Outline malaria parasites and classify them by life-cycle stage.
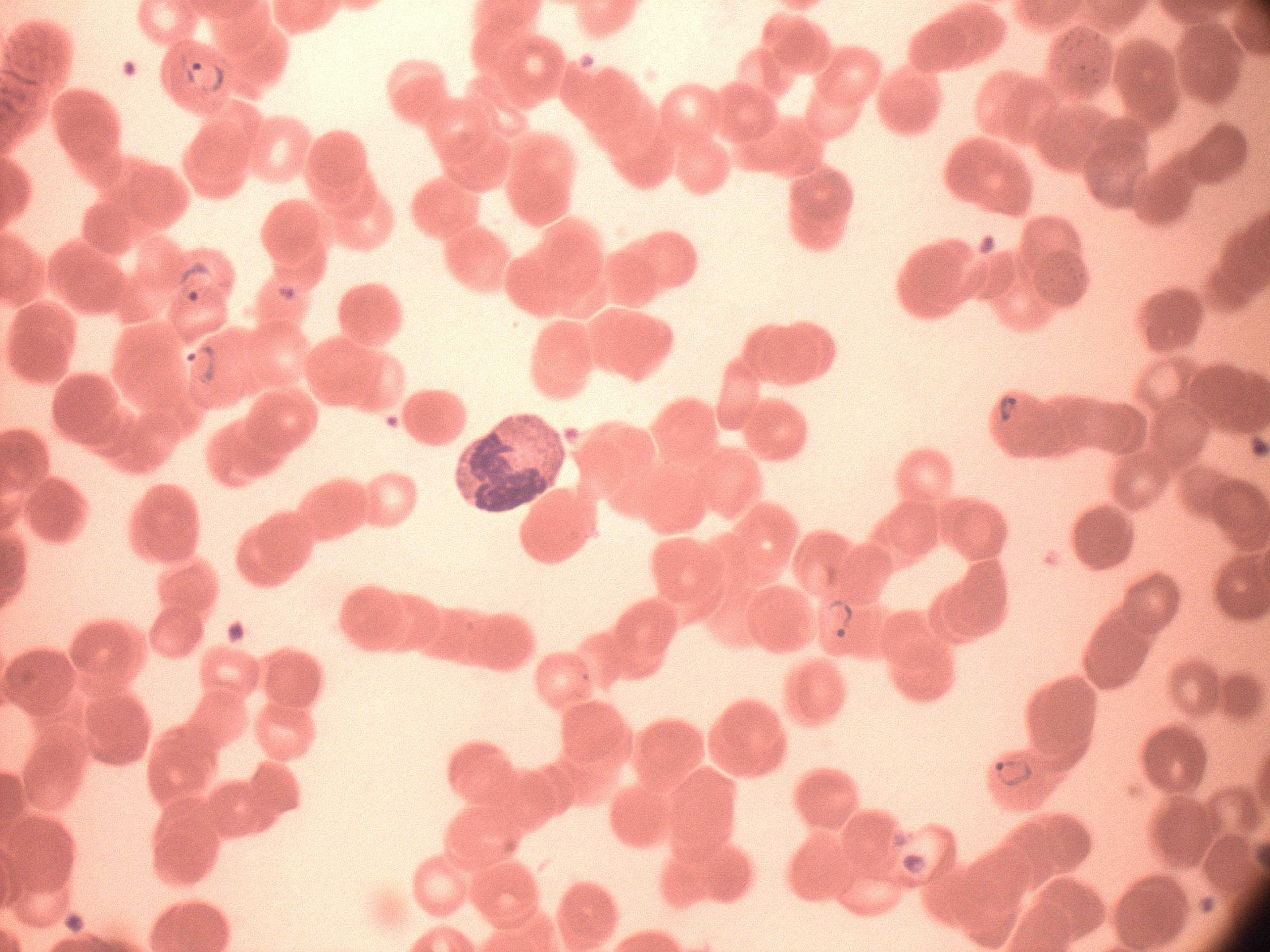
Approximate bounding boxes as (x1,y1)-(x2,y2) corner pairs in pixels, from the source annotation, which is not necessarily exhaustive.
Ring forms: (172,44)-(238,104), (172,255)-(223,310), (178,338)-(223,392), (991,388)-(1023,426), (819,589)-(857,651), (983,748)-(1039,793).

One field from this slide. Species: Plasmodium falciparum. Thin blood smear. Giemsa stain. 100x magnification. Image is 1270×952 pixels. Leica DM2000 optical microscope with a built-in camera.